Report the malaria status of this cell.
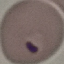
It is parasitized.

stain = Giemsa
image type = automatically extracted cell patch, resized to 64 × 64 pixels
preparation = thin blood smear
capture = smartphone camera at the microscope eyepiece